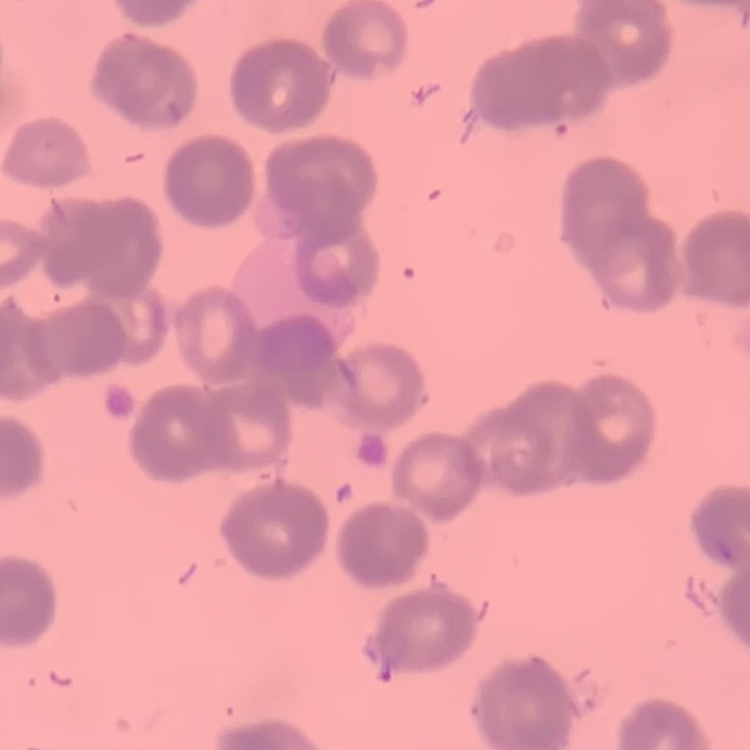

The red blood cells exhibit rouleaux formation. Thin blood film. One tile cut from a larger photomicrograph. Stained with either Field's or Giemsa.